Draw a bounding box around every parasitised red blood cell, every trophozoite, every gametocyte, every leukocyte, and every artifact (platelet-like body, stain precipitate, or debris).
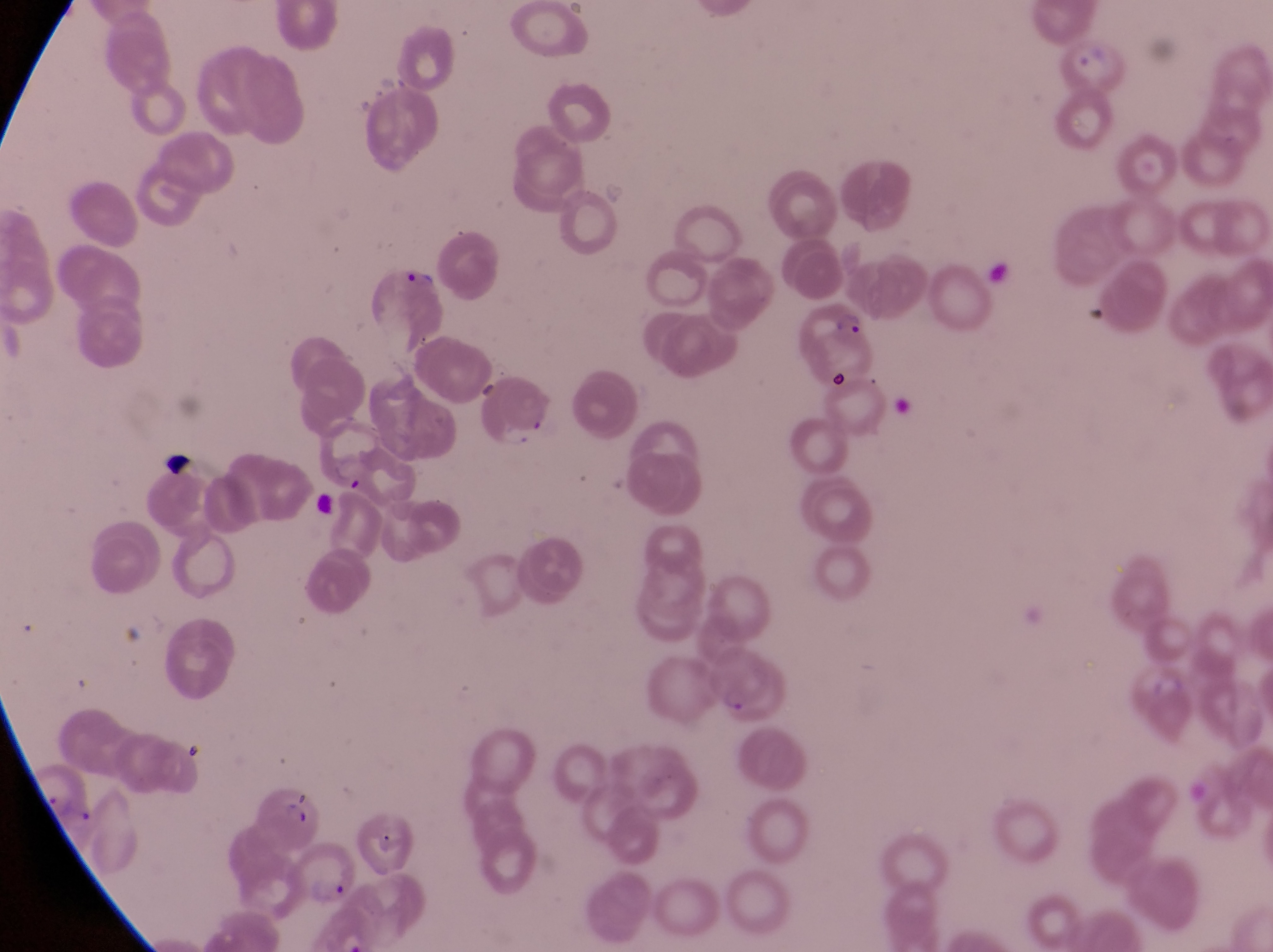
Approximate bounding boxes as [left, top, right, bottom] in pixels.
Parasitised red blood cells: [1069, 39, 1127, 94], [345, 264, 444, 347], [808, 295, 873, 373], [714, 647, 784, 726], [252, 784, 321, 851], [294, 841, 366, 909].
No leukocytes observed.
Artifacts (platelet-like body, stain precipitate, or debris): [988, 248, 1013, 300], [158, 442, 195, 481].

Thin blood smear. Single field of view. Image is 1273×952 pixels. Captured by a smartphone held over the eyepiece of an Olympus CX-23 microscope. Collected in Uganda. At a magnification of 1000x.